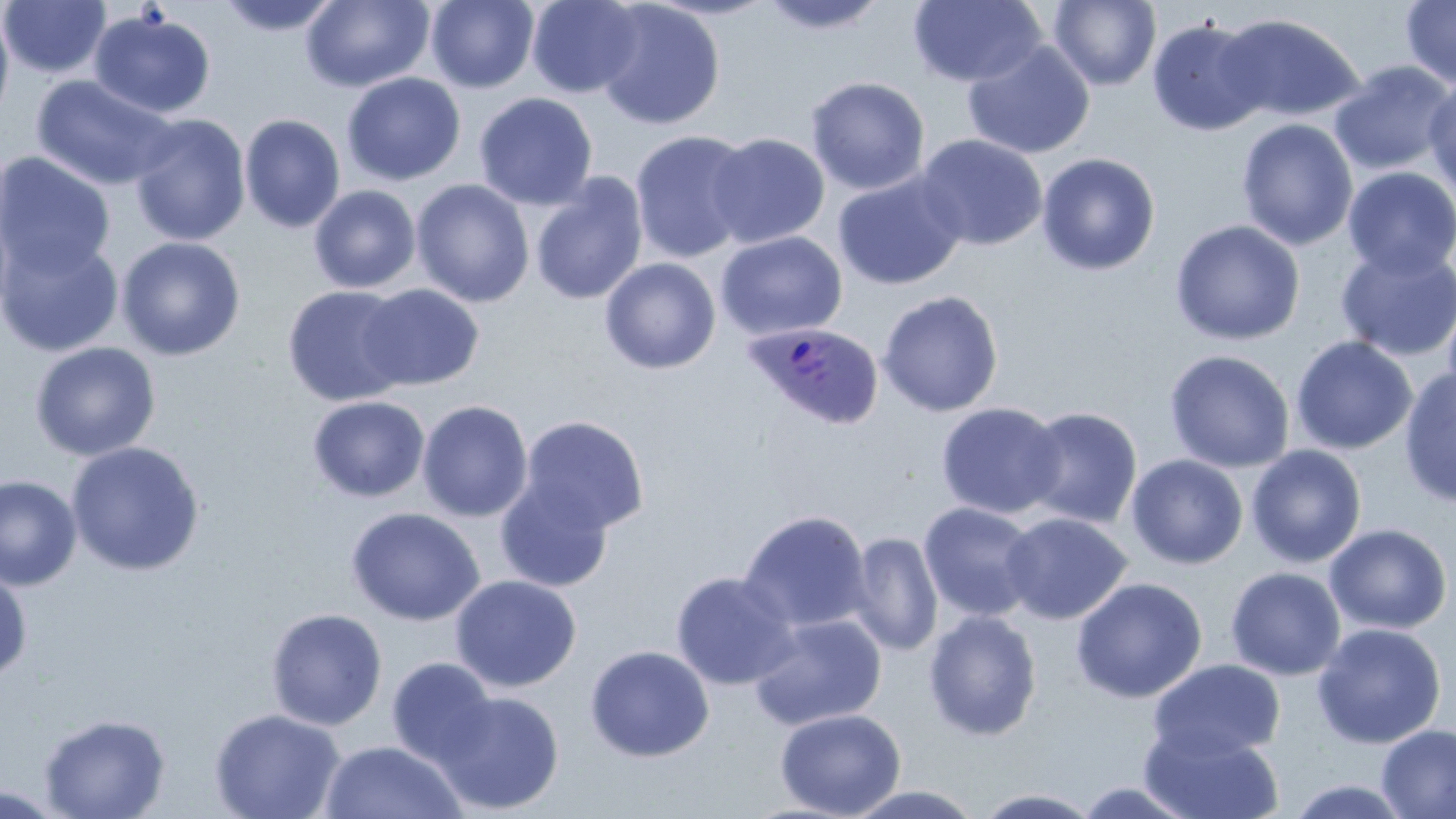

Summary:
  - Coordinate format: approximate bounding boxes as (x1,y1)-(x2,y2) corner pairs in pixels
  - Uninfected red blood cell locations: (1,0)-(111,78), (216,0)-(343,36), (301,0)-(434,92), (526,0)-(646,98), (758,0)-(890,35), (908,0)-(1046,88), (1048,0)-(1162,90), (1401,0)-(1456,89), (425,1)-(540,93), (595,1)-(725,130), (0,2)-(15,132), (88,9)-(216,119), (1216,12)-(1364,122), (1146,17)-(1271,137), (962,39)-(1095,159), (1328,60)-(1455,176), (341,72)-(466,186), (31,74)-(179,191), (1424,75)-(1456,200), (805,76)-(930,195), (340,84)-(595,195), (474,92)-(598,210), (239,113)-(346,233), (129,114)-(251,247), (1237,118)-(1358,251), (629,129)-(755,264), (707,133)-(829,249), (914,134)-(1049,251), (0,152)-(116,278), (1036,153)-(1160,276), (1342,166)-(1456,280), (833,171)-(966,290), (529,172)-(648,306), (411,179)-(534,308), (309,184)-(421,293), (0,205)-(16,329), (1169,220)-(1306,345), (715,231)-(848,341), (0,232)-(124,358), (116,236)-(246,361), (1335,243)-(1456,362), (599,258)-(721,374), (358,283)-(484,391), (282,285)-(412,407), (878,290)-(1003,417), (1441,292)-(1456,412), (1290,335)-(1418,455), (29,341)-(161,462), (1164,349)-(1295,473), (1399,368)-(1456,508), (307,395)-(430,502), (417,400)-(534,522), (936,401)-(1066,519), (1021,406)-(1143,528), (518,415)-(650,535), (66,441)-(205,576), (1246,444)-(1367,568), (1126,454)-(1248,570), (494,474)-(614,593), (0,475)-(82,591), (919,501)-(1040,621), (346,507)-(485,626), (738,510)-(872,633), (1001,512)-(1132,625), (1324,523)-(1452,635), (848,531)-(943,656), (0,566)-(32,683), (1226,567)-(1346,680), (670,570)-(798,690), (449,575)-(582,692), (1071,577)-(1208,703), (265,608)-(387,730), (923,610)-(1042,741), (749,613)-(887,730), (1312,622)-(1447,749), (584,644)-(715,762), (386,657)-(498,769), (1148,659)-(1286,762), (433,689)-(565,815), (774,707)-(906,818), (210,709)-(346,818), (39,713)-(170,819), (1140,724)-(1286,819), (1376,724)-(1456,818), (319,739)-(467,819), (1287,778)-(1413,818), (1073,780)-(1200,817), (0,785)-(73,819), (844,785)-(984,818), (973,787)-(1103,818)
  - Plasmodium ovale-infected red blood cell locations: (743,322)-(884,429)
  - Slide-level diagnosis: Plasmodium ovale
  - Field of view: single
  - Preparation: thin blood film
  - Image size: 1456×819 pixels
  - Stain: May-Grünwald-Giemsa
  - Magnification: 1000x
  - Modality: light microscopy